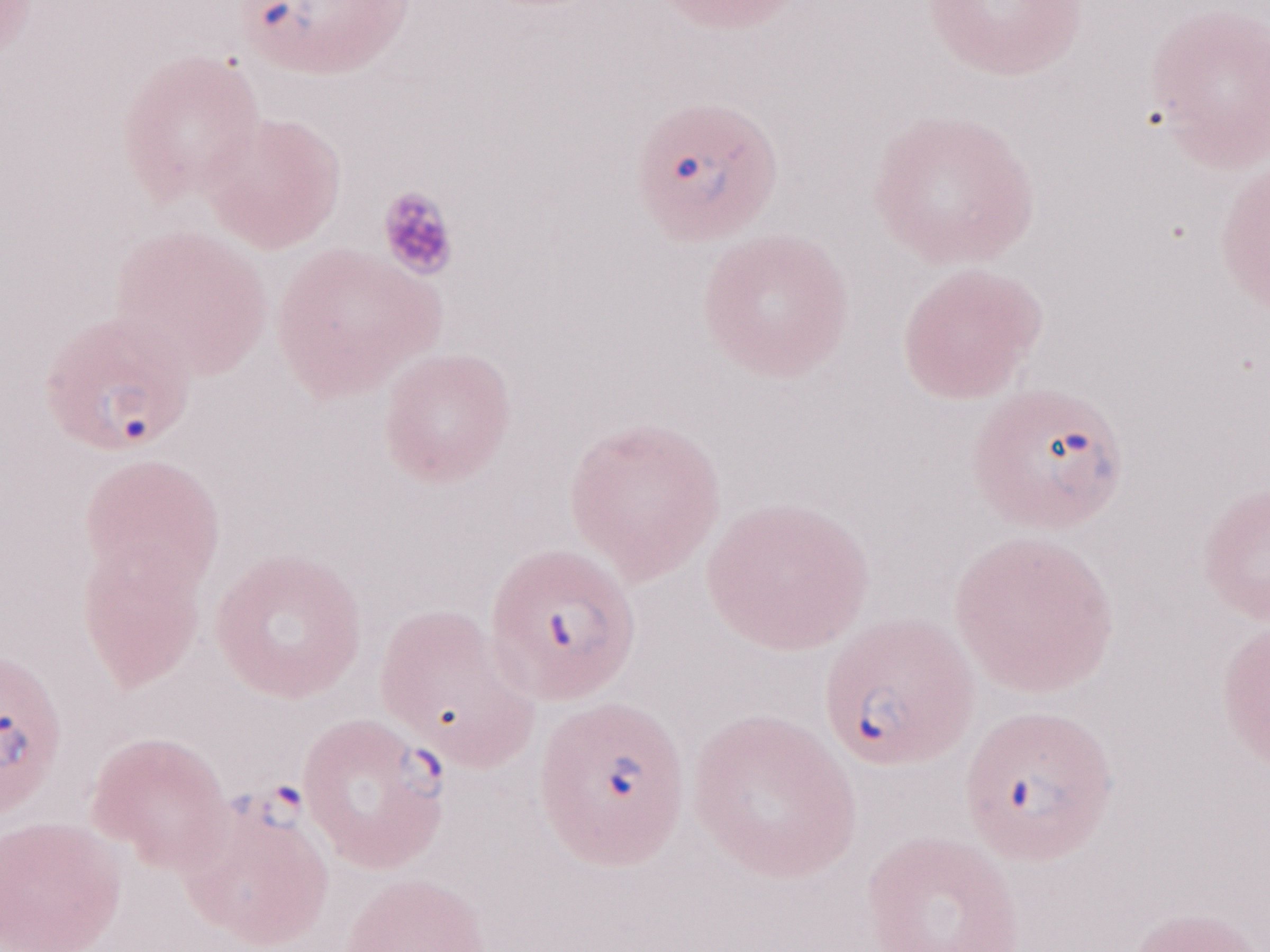
May-Grünwald-Giemsa-stained preparation. Image is 1270×952 pixels. Thin blood smear. Olympus BX43 microscope and DP73 digital camera. Malaria diagnosis (patient-level): positive. Magnification: 1,000x. Single field of view.